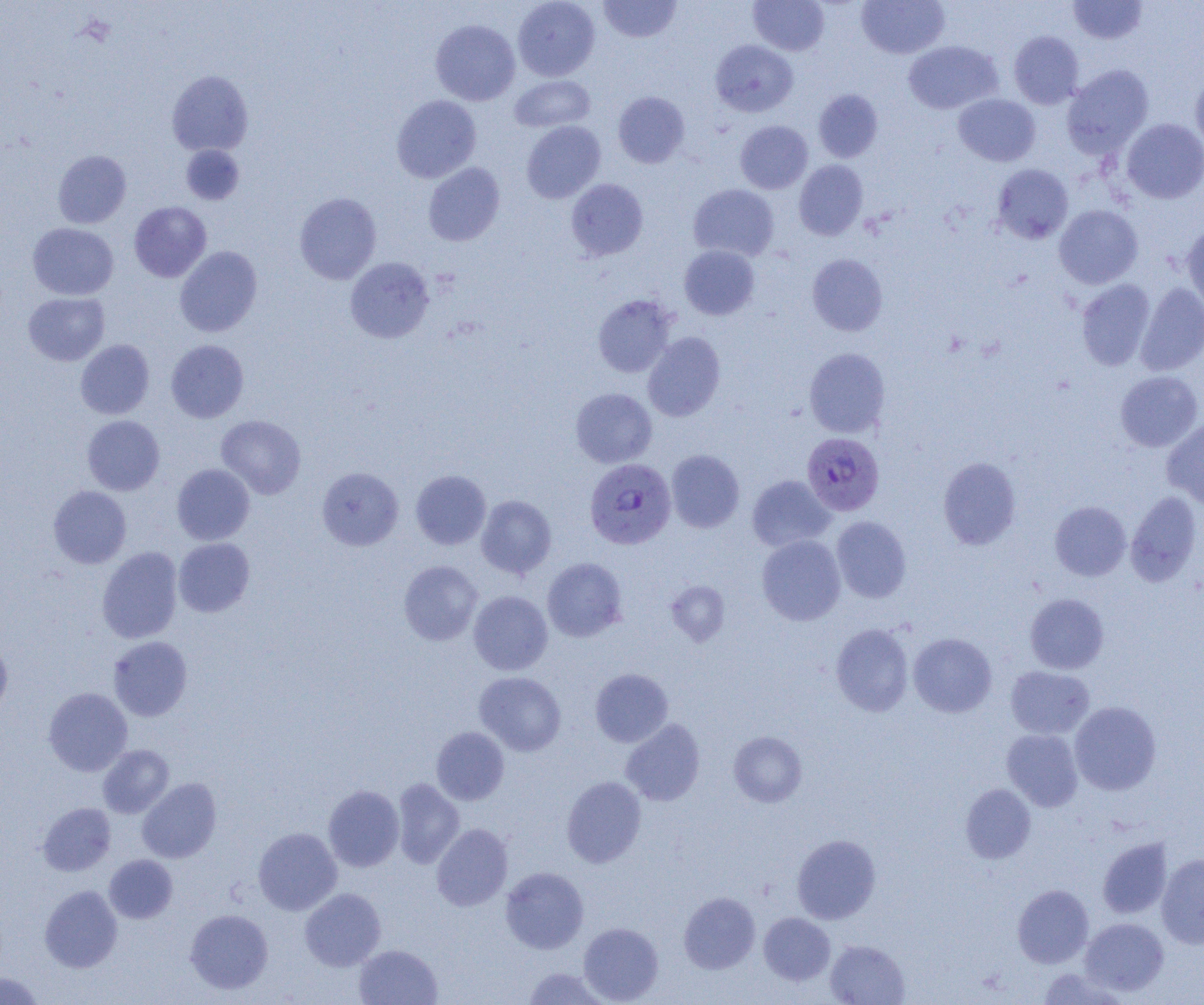
Approximate bounding boxes as (x1,y1)-(x2,y2) corner pairs in pixels. Uninfected red blood cell locations: (513,0)-(600,81), (598,0)-(682,43), (748,0)-(829,55), (856,0)-(949,59), (1068,0)-(1148,45), (430,19)-(520,105), (1009,31)-(1083,109), (710,40)-(798,117), (903,41)-(1003,114), (1062,64)-(1154,157), (167,70)-(253,156), (1190,72)-(1204,155), (510,75)-(595,132), (813,89)-(883,162), (613,91)-(689,168), (953,94)-(1040,166), (392,95)-(481,183), (1121,118)-(1204,204), (521,120)-(606,203), (735,121)-(813,194), (181,145)-(245,205), (53,150)-(131,228), (794,160)-(868,240), (423,162)-(505,246), (992,164)-(1073,244), (565,179)-(648,260), (688,184)-(779,261), (294,192)-(382,284), (129,201)-(211,282), (1054,204)-(1143,288), (1182,222)-(1204,312), (27,223)-(119,300), (679,245)-(760,320), (175,246)-(262,337), (807,254)-(888,336), (345,257)-(434,343), (1076,279)-(1155,370), (1136,282)-(1204,375), (23,292)-(110,366), (593,294)-(677,378), (643,331)-(725,421), (75,339)-(154,419), (166,340)-(249,422), (804,347)-(890,437), (1115,370)-(1203,452), (571,388)-(657,467), (82,415)-(164,495), (216,415)-(306,499), (1162,418)-(1204,508), (666,449)-(744,533), (938,457)-(1021,550), (172,464)-(255,545), (317,467)-(403,550), (411,470)-(491,549), (747,475)-(835,552), (48,486)-(131,569), (1126,490)-(1202,586), (476,495)-(556,578), (1050,501)-(1131,581), (831,516)-(911,603), (756,534)-(846,625), (174,538)-(255,617), (97,547)-(183,644), (542,557)-(627,642), (398,560)-(483,646), (666,580)-(730,646), (469,591)-(552,675), (1024,593)-(1109,674), (831,623)-(914,716), (908,633)-(996,717), (0,635)-(13,720), (108,636)-(192,721), (1005,666)-(1094,739), (590,668)-(673,747), (474,671)-(566,756), (43,687)-(132,776), (1069,701)-(1161,795), (621,719)-(705,806), (431,727)-(509,805), (1002,729)-(1083,811), (728,731)-(807,807), (98,745)-(174,818), (562,776)-(646,867), (137,778)-(221,863), (392,778)-(465,869), (960,783)-(1036,864), (323,785)-(404,871), (38,802)-(116,876), (431,823)-(513,911), (253,827)-(342,915), (792,834)-(881,924), (1098,838)-(1173,919), (1156,854)-(1204,949), (104,855)-(178,923), (500,866)-(589,954), (1012,884)-(1093,968), (40,885)-(123,972), (300,888)-(385,971), (679,891)-(760,973), (185,908)-(273,994), (759,912)-(835,985), (1080,917)-(1169,996), (578,922)-(664,1004), (825,939)-(910,1005), (354,944)-(442,1005), (522,967)-(612,1004), (1037,968)-(1126,1004), (0,972)-(45,1004). Plasmodium falciparum-infected red blood cell locations: (802,433)-(884,515), (584,458)-(676,550). Slide-level diagnosis: Plasmodium falciparum. Image is 1204×1005 pixels. Optical microscopy. 1000x magnification. Thin blood smear. Single field of view.